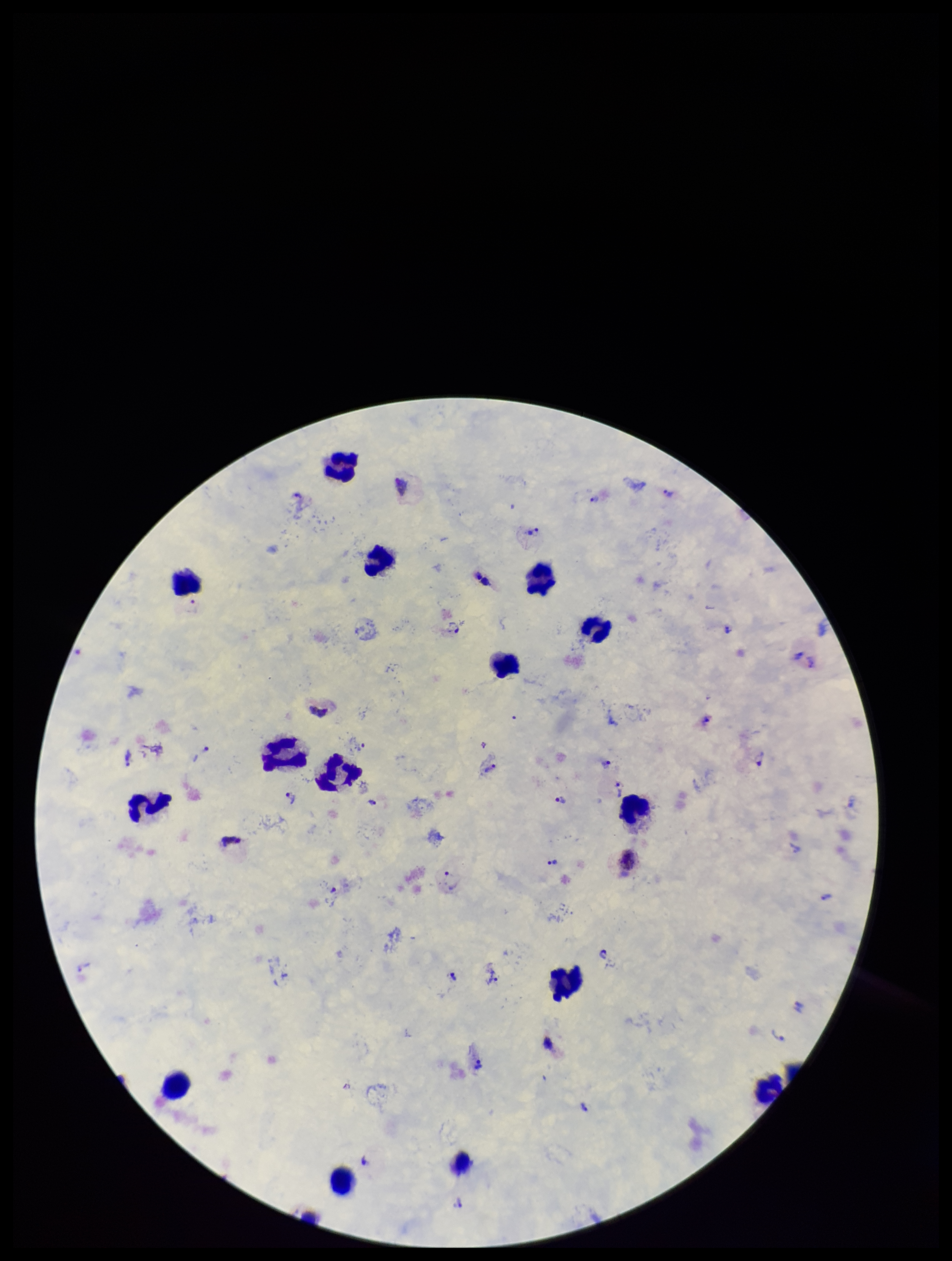

preparation = thick smear
stain = Giemsa
leukocyte count = 15
patient malaria status = positive
parasite count = 20
field of view = single
image size = 952×1261 pixels
capture = smartphone photograph through the microscope eyepiece
Plasmodium parasites = seen
species reported for this patient = Plasmodium vivax